Classify this cell by malaria status.
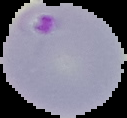

Parasitized.

Summary:
  - Preparation: thin blood smear
  - Image type: segmented cell region on a black background
  - Image size: 127×118 pixels